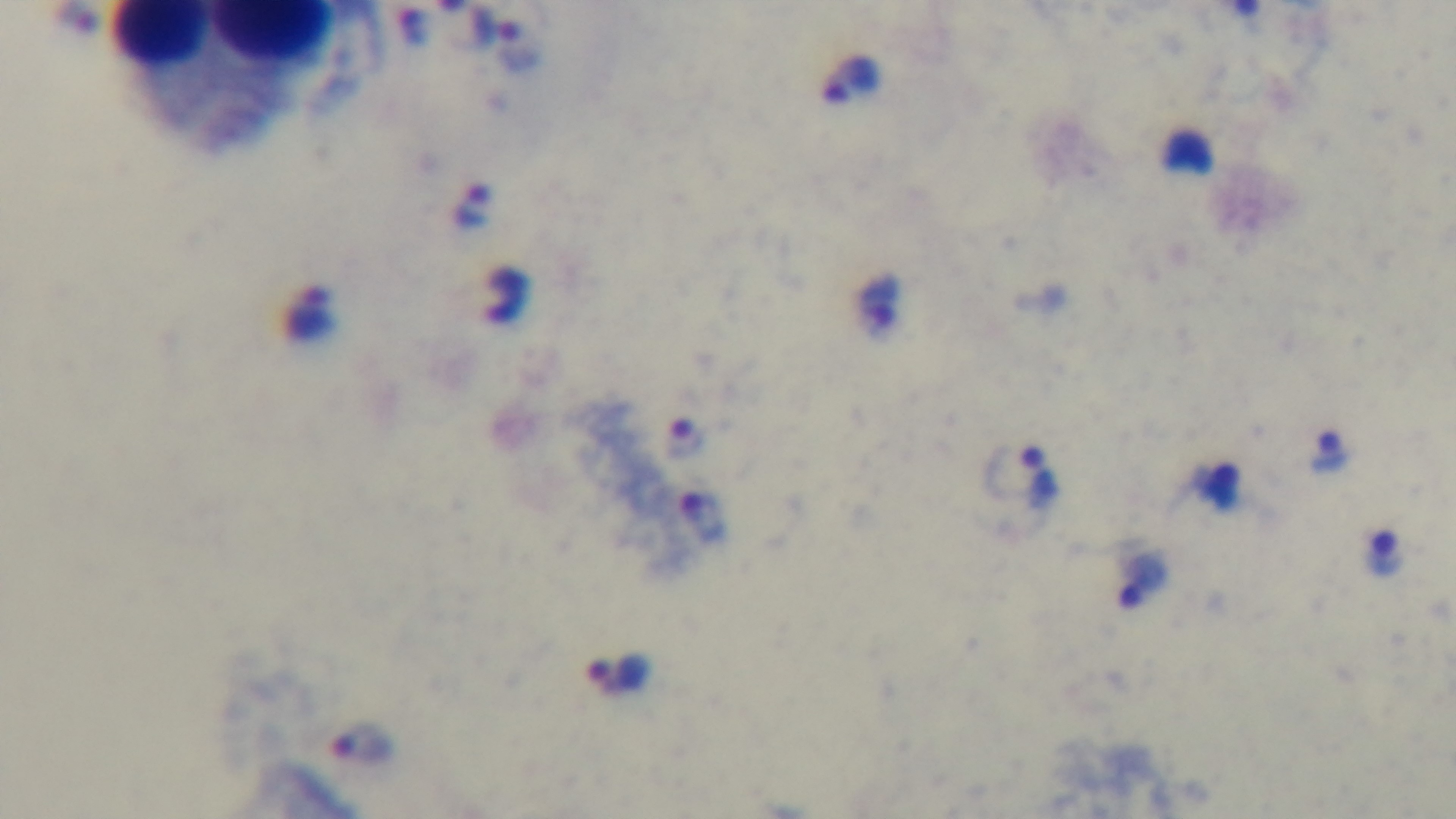

malaria status = infected
modality = light microscopy
field of view = single
objective = 100x oil immersion
capture = mounted 4K digital camera
preparation = thick smear
stain = Giemsa